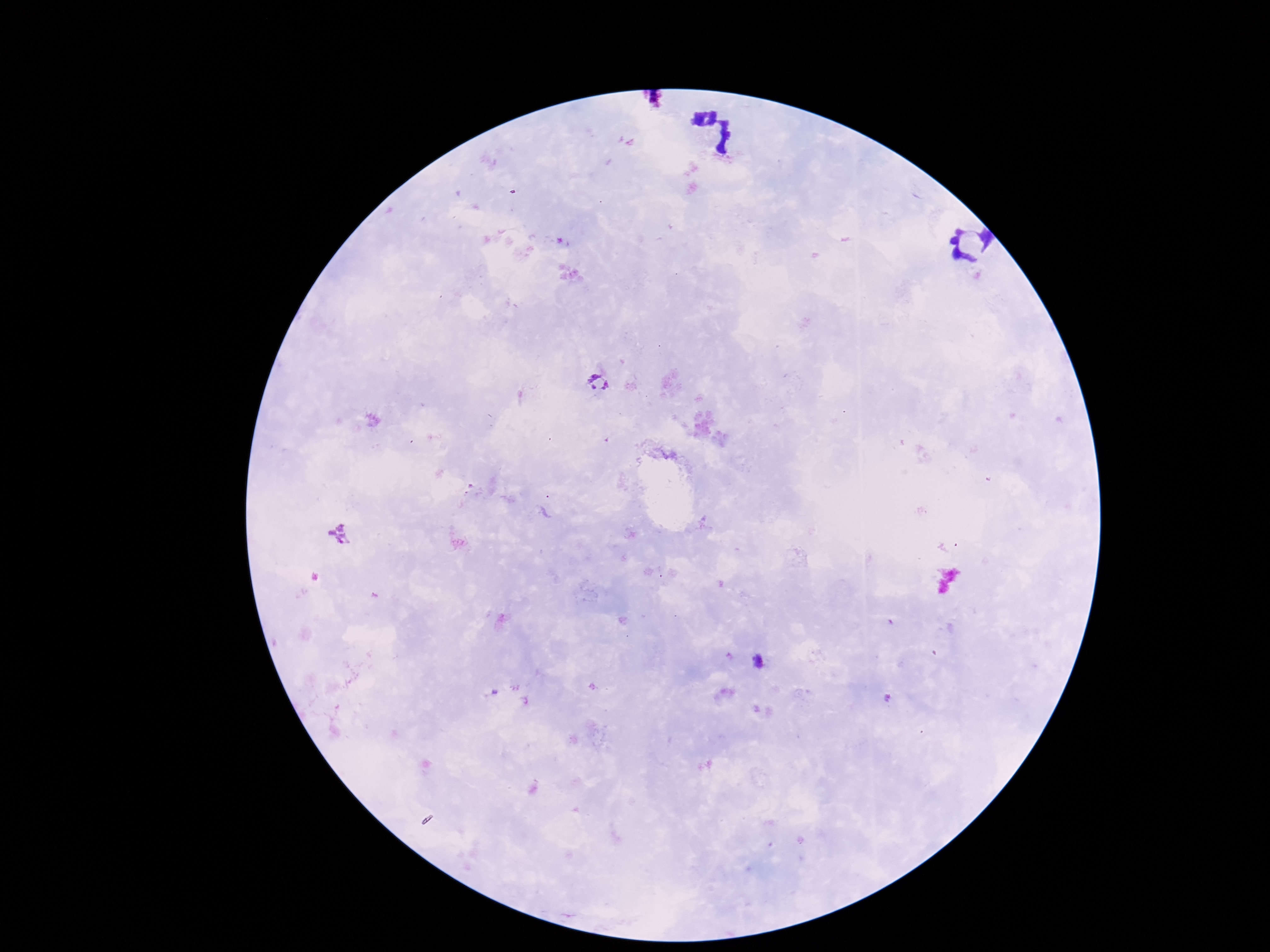

Approximate object centers, in pixels from the top-left corner.
Summary:
  - Plasmodium parasite locations: (x=600, y=388), (x=339, y=534), (x=757, y=662)
  - Field of view: one from this slide
  - Stain: Giemsa
  - Patient malaria status: positive
  - Capture: smartphone camera through the microscope eyepiece
  - Magnification: 100x
  - Preparation: thick blood smear
  - Image size: 1270×952 pixels